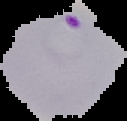

Result: Plasmodium parasites detected. From a thin blood film. Image is 127×121 pixels. The area outside the segmented cell region is set to black.